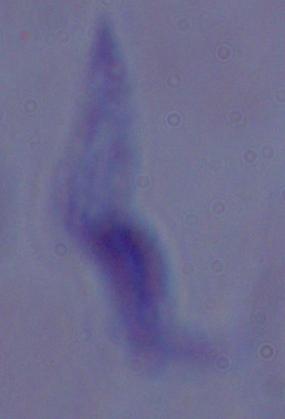 A trypanosome is seen. Captured at 1000x magnification. Photomicrograph.